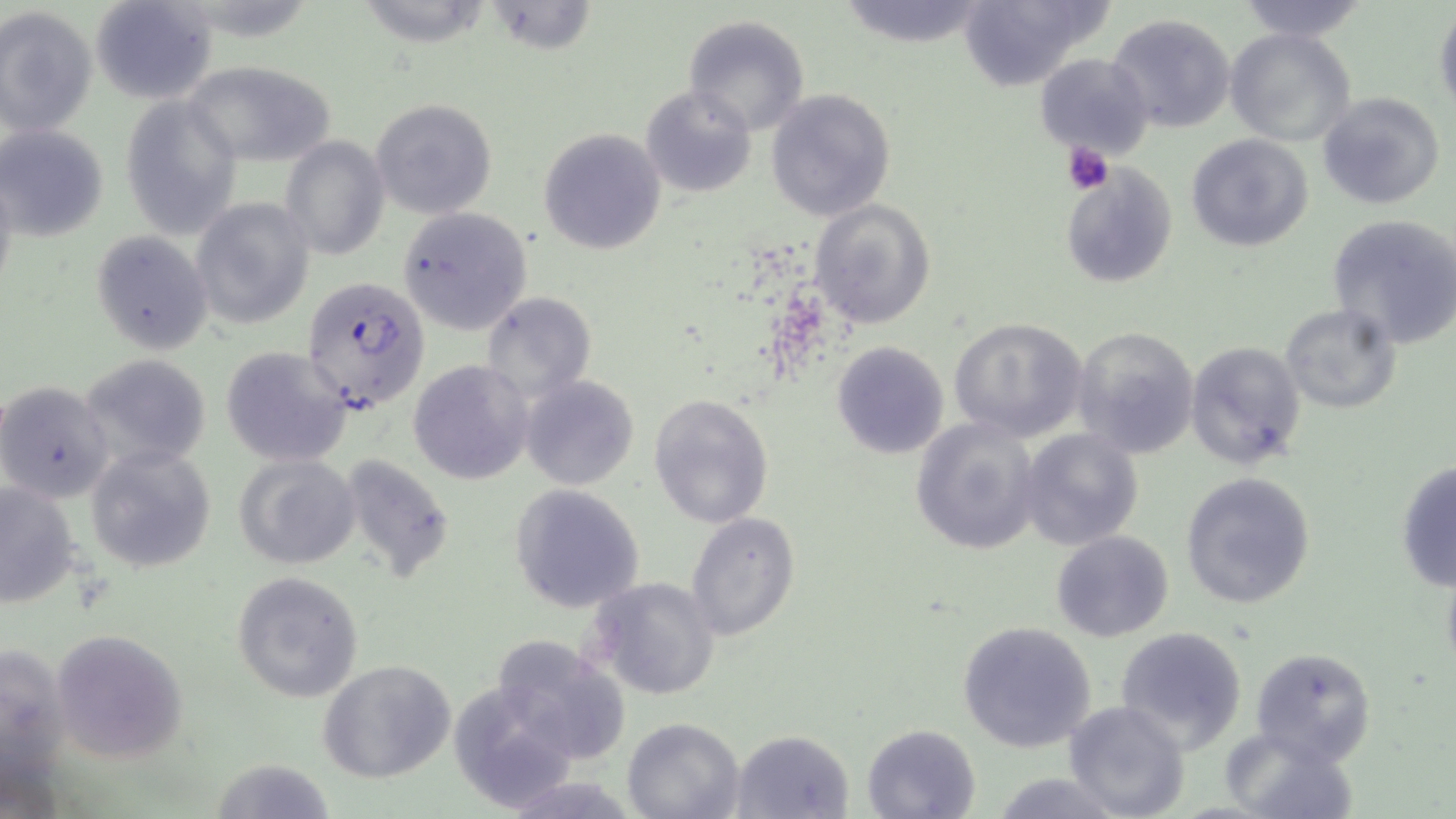
Summary:
  - Coordinate format: approximate bounding boxes as (x1, y1, x2, y2) in pixels
  - Plasmodium falciparum-infected red blood cell locations: (302, 277, 431, 413)
  - Uninfected red blood cell locations: (90, 0, 218, 105), (362, 0, 489, 60), (834, 0, 995, 49), (956, 0, 1110, 91), (1234, 0, 1370, 41), (493, 4, 602, 54), (1433, 5, 1456, 119), (0, 6, 97, 139), (1107, 13, 1236, 133), (683, 14, 812, 137), (1226, 26, 1357, 148), (1035, 52, 1154, 159), (181, 60, 339, 167), (641, 85, 757, 199), (766, 88, 896, 223), (1316, 90, 1446, 211), (121, 96, 243, 236), (371, 97, 498, 220), (2, 123, 109, 242), (539, 128, 666, 254), (1186, 133, 1314, 252), (280, 135, 390, 261), (1059, 163, 1176, 291), (191, 196, 315, 329), (808, 198, 937, 328), (398, 208, 532, 334), (1327, 213, 1456, 349), (92, 231, 213, 353), (480, 291, 596, 407), (1279, 304, 1403, 416), (949, 317, 1088, 443), (1072, 325, 1201, 459), (1184, 340, 1306, 469), (831, 341, 949, 459), (220, 344, 351, 467), (78, 354, 212, 474), (409, 361, 531, 483), (520, 376, 640, 491), (0, 380, 114, 503), (649, 392, 776, 528), (910, 416, 1042, 556), (1017, 427, 1143, 550), (85, 444, 219, 574), (234, 453, 361, 570), (338, 454, 457, 582), (1395, 461, 1456, 594), (1179, 472, 1317, 610), (0, 478, 85, 606), (509, 484, 646, 612), (686, 511, 801, 641), (1050, 530, 1175, 643), (231, 571, 364, 702), (585, 577, 722, 701), (957, 622, 1098, 753), (1114, 626, 1248, 752), (50, 628, 188, 762), (487, 634, 629, 769), (1, 641, 72, 801), (1249, 646, 1378, 768), (319, 660, 458, 784), (447, 682, 584, 813), (1062, 700, 1191, 819), (622, 717, 745, 819), (861, 723, 983, 818), (1223, 728, 1355, 819), (732, 729, 854, 818), (214, 753, 336, 819), (512, 772, 642, 819)
  - Platelet locations: (1062, 140, 1114, 196)
  - Slide-level diagnosis: Plasmodium falciparum
  - Magnification: 1000x
  - Preparation: thin blood film
  - Modality: light microscopy
  - Field of view: one of a larger specimen
  - Image size: 1456×819 pixels
  - Stain: May-Grünwald-Giemsa